Identify the parasite.
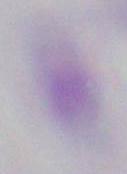

This is Toxoplasma gondii.

Summary:
  - Magnification: 1000x
  - Modality: photomicrograph